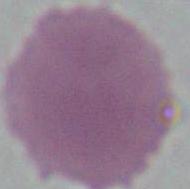

Summary:
  - Modality: photomicrograph
  - Identification: erythrocyte
  - Magnification: 1000x